Identify the parasite.
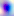

This is Toxoplasma gondii.

Summary:
  - Magnification: 400x
  - Modality: photomicrograph